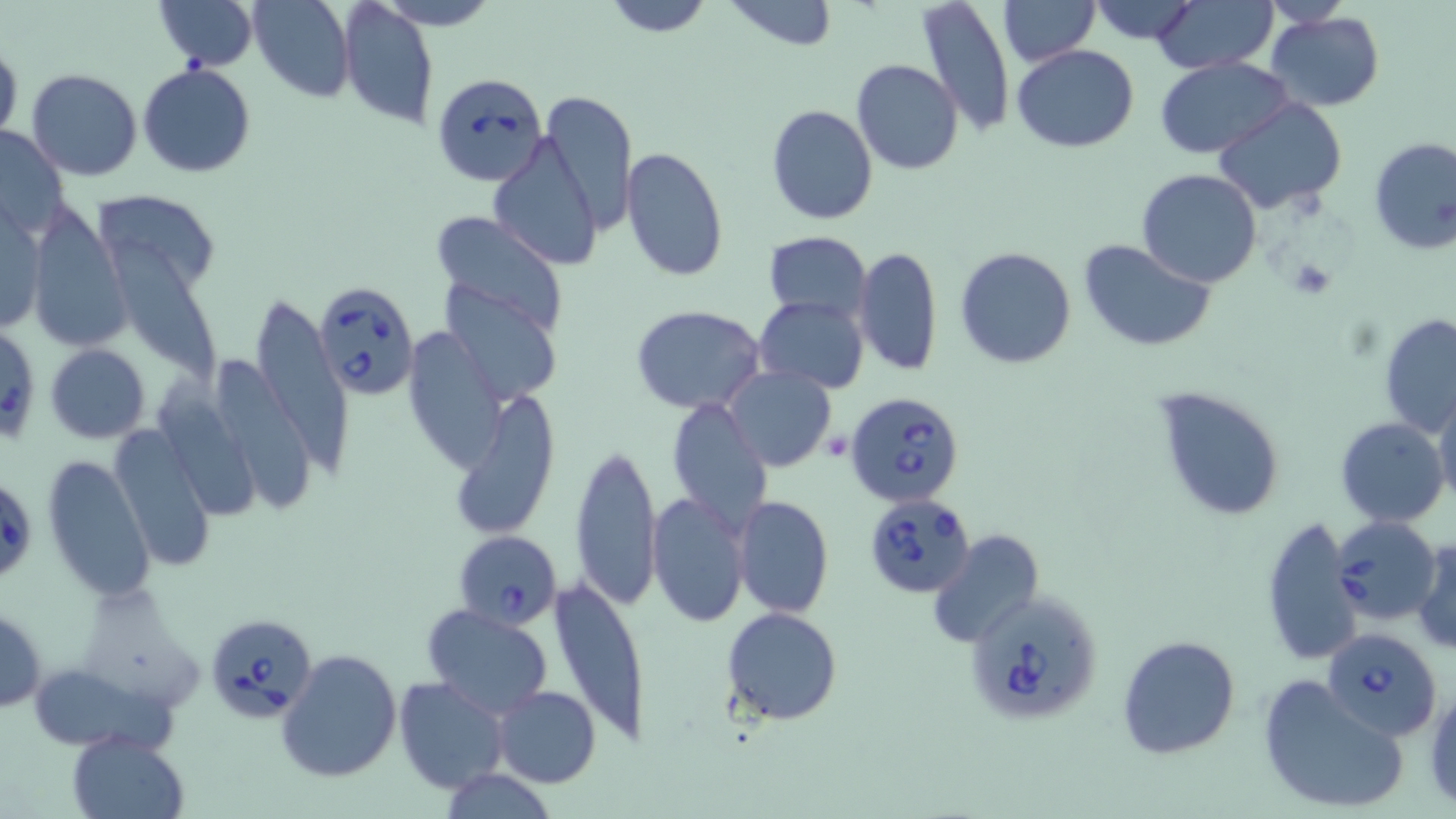
Approximate bounding boxes as named x1/y1/x2/y2 corners in pixels. Uninfected red blood cell locations: (x1=152, y1=0, x2=258, y2=70), (x1=249, y1=0, x2=356, y2=101), (x1=374, y1=0, x2=500, y2=31), (x1=720, y1=0, x2=840, y2=50), (x1=915, y1=0, x2=1016, y2=137), (x1=1086, y1=0, x2=1202, y2=47), (x1=1151, y1=0, x2=1276, y2=72), (x1=1263, y1=0, x2=1357, y2=28), (x1=602, y1=1, x2=712, y2=37), (x1=998, y1=1, x2=1099, y2=66), (x1=339, y1=2, x2=439, y2=131), (x1=1265, y1=12, x2=1385, y2=111), (x1=0, y1=42, x2=22, y2=146), (x1=1012, y1=44, x2=1140, y2=154), (x1=1156, y1=56, x2=1293, y2=159), (x1=852, y1=59, x2=962, y2=174), (x1=138, y1=63, x2=256, y2=177), (x1=26, y1=68, x2=142, y2=180), (x1=538, y1=89, x2=637, y2=234), (x1=1212, y1=97, x2=1350, y2=216), (x1=765, y1=103, x2=880, y2=225), (x1=1, y1=125, x2=70, y2=238), (x1=489, y1=136, x2=602, y2=269), (x1=1367, y1=137, x2=1456, y2=257), (x1=619, y1=147, x2=731, y2=284), (x1=1136, y1=169, x2=1263, y2=288), (x1=93, y1=193, x2=224, y2=286), (x1=29, y1=206, x2=128, y2=353), (x1=0, y1=207, x2=46, y2=338), (x1=429, y1=210, x2=567, y2=339), (x1=103, y1=224, x2=224, y2=391), (x1=763, y1=232, x2=871, y2=322), (x1=1081, y1=238, x2=1215, y2=352), (x1=854, y1=246, x2=944, y2=376), (x1=954, y1=246, x2=1077, y2=369), (x1=444, y1=283, x2=561, y2=406), (x1=252, y1=291, x2=350, y2=478), (x1=754, y1=296, x2=870, y2=392), (x1=630, y1=305, x2=768, y2=415), (x1=1378, y1=313, x2=1456, y2=439), (x1=409, y1=327, x2=515, y2=470), (x1=44, y1=343, x2=149, y2=442), (x1=215, y1=357, x2=314, y2=511), (x1=724, y1=365, x2=839, y2=473), (x1=159, y1=385, x2=264, y2=525), (x1=448, y1=386, x2=562, y2=541), (x1=1155, y1=387, x2=1287, y2=521), (x1=1431, y1=388, x2=1456, y2=508), (x1=666, y1=396, x2=774, y2=533), (x1=1335, y1=416, x2=1449, y2=528), (x1=108, y1=424, x2=218, y2=570), (x1=569, y1=441, x2=660, y2=609), (x1=42, y1=455, x2=156, y2=601), (x1=647, y1=492, x2=752, y2=628), (x1=731, y1=494, x2=834, y2=618), (x1=1258, y1=517, x2=1361, y2=664), (x1=926, y1=528, x2=1045, y2=647), (x1=1413, y1=537, x2=1455, y2=656), (x1=549, y1=574, x2=651, y2=748), (x1=422, y1=603, x2=552, y2=717), (x1=1, y1=606, x2=46, y2=713), (x1=722, y1=606, x2=843, y2=724), (x1=1116, y1=635, x2=1240, y2=758), (x1=276, y1=648, x2=403, y2=781), (x1=1257, y1=674, x2=1410, y2=817), (x1=393, y1=675, x2=510, y2=795), (x1=1424, y1=678, x2=1456, y2=808), (x1=491, y1=686, x2=602, y2=787), (x1=68, y1=730, x2=187, y2=818), (x1=437, y1=766, x2=556, y2=819). Platelet locations: (x1=1284, y1=256, x2=1339, y2=301). Babesia divergens-infected red blood cell locations: (x1=433, y1=71, x2=548, y2=185), (x1=315, y1=281, x2=420, y2=400), (x1=0, y1=324, x2=41, y2=446), (x1=846, y1=391, x2=965, y2=509), (x1=1, y1=487, x2=33, y2=578), (x1=864, y1=490, x2=977, y2=597), (x1=1334, y1=516, x2=1441, y2=626), (x1=454, y1=530, x2=562, y2=631), (x1=964, y1=590, x2=1103, y2=726), (x1=206, y1=614, x2=315, y2=723), (x1=1321, y1=627, x2=1442, y2=741). Slide-level diagnosis: Babesia divergens. Optical microscopy. Thin blood film. May-Grünwald-Giemsa stain. Image is 1456×819 pixels. One field of a larger specimen. 1000x magnification.